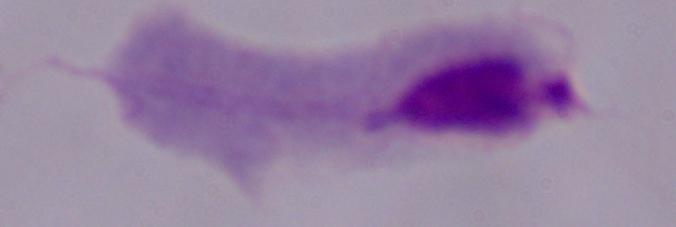
Summary:
  - Identification: trichomonad
  - Modality: micrograph
  - Magnification: 1000x